Point out each Plasmodium parasite.
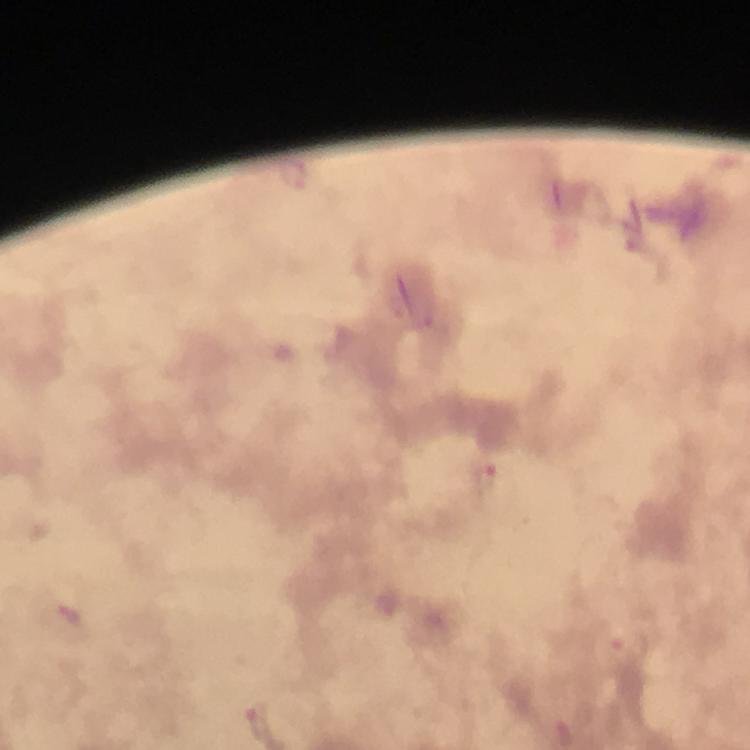

Approximate object centers, in pixels from the top-left corner.
Plasmodium parasites: (x=294, y=174), (x=486, y=478), (x=69, y=613), (x=632, y=644).

Photographed with a smartphone mounted on the microscope. Thick blood smear. At 100x magnification. Giemsa-stained preparation. Image is 750×750 pixels. Immersion oil was used. From a diagnostic examination for malaria. Cropped region of a single field of view.